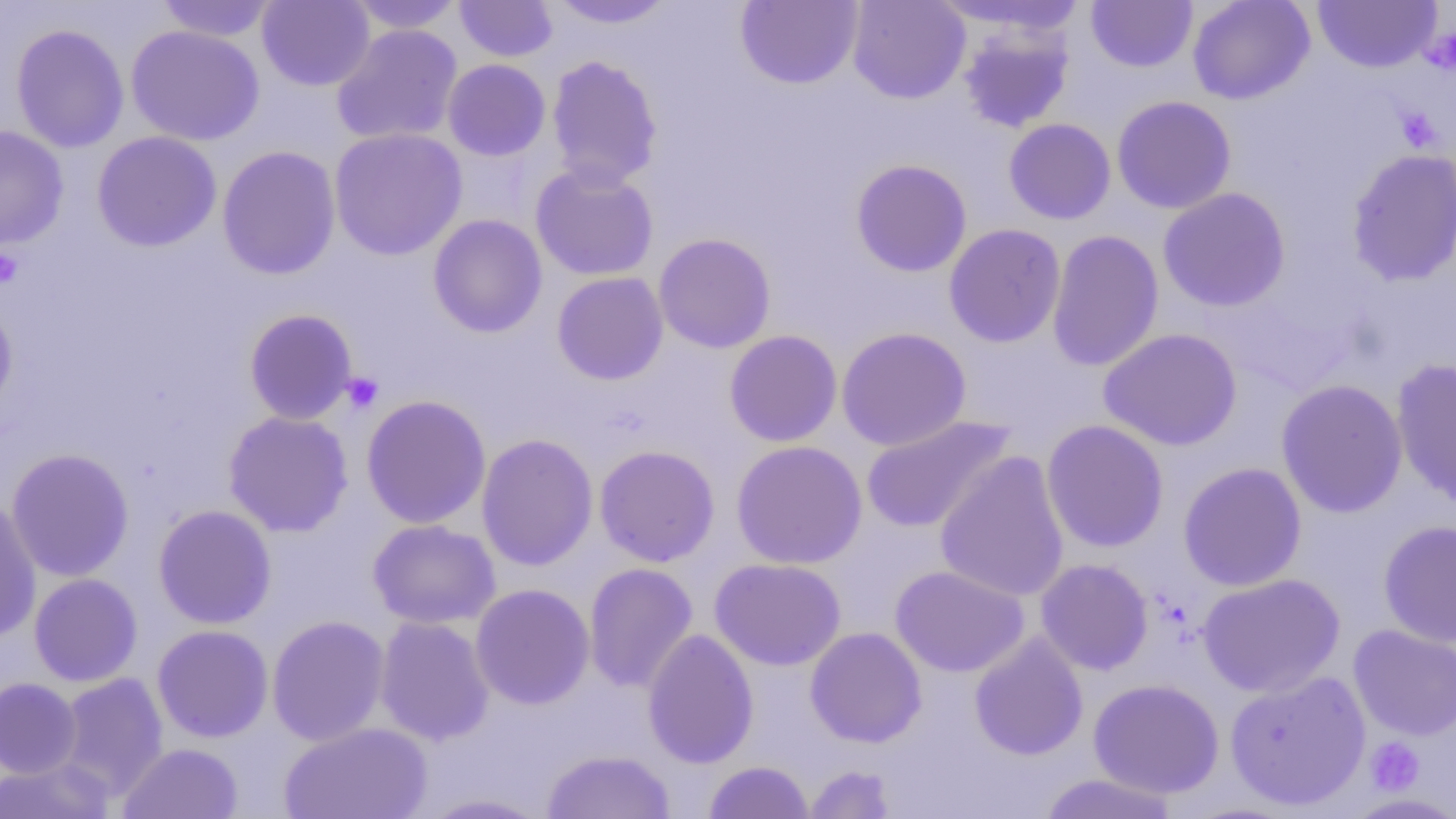

slide-level diagnosis = negative for blood parasites
platelet locations = approximate bounding boxes as (x1, y1, x2, y2) in pixels: (1422, 26, 1456, 75), (1395, 107, 1444, 152), (0, 248, 24, 289), (340, 371, 383, 414), (1365, 737, 1425, 795)
image size = 1456×819 pixels
preparation = thin blood film
uninfected red blood cell locations = approximate bounding boxes as (x1, y1, x2, y2) in pixels: (155, 0, 279, 42), (257, 0, 375, 91), (345, 0, 466, 33), (455, 0, 558, 62), (735, 0, 863, 89), (847, 0, 970, 104), (931, 0, 1093, 37), (1187, 0, 1315, 105), (1312, 0, 1442, 72), (548, 1, 677, 29), (1086, 1, 1197, 72), (11, 23, 129, 153), (957, 23, 1075, 133), (331, 24, 463, 146), (126, 25, 265, 146), (546, 55, 663, 190), (442, 59, 551, 161), (1111, 95, 1236, 214), (1003, 118, 1116, 224), (0, 125, 69, 250), (329, 128, 467, 261), (92, 131, 222, 252), (217, 145, 341, 280), (1345, 148, 1456, 286), (850, 158, 972, 277), (530, 163, 659, 281), (1158, 187, 1291, 312), (428, 214, 547, 338), (943, 223, 1066, 347), (1046, 229, 1164, 372), (653, 232, 776, 353), (552, 272, 669, 385), (0, 299, 18, 417), (244, 309, 358, 425), (836, 327, 971, 451), (1098, 328, 1242, 451), (724, 330, 842, 447), (1390, 357, 1456, 511), (1276, 379, 1408, 518), (361, 394, 492, 529), (223, 410, 354, 537), (860, 415, 1016, 534), (1041, 419, 1169, 553), (476, 433, 598, 571), (731, 440, 867, 569), (594, 444, 720, 567), (6, 448, 135, 582), (934, 450, 1070, 602), (1178, 462, 1307, 591), (0, 497, 42, 642), (153, 505, 277, 629), (368, 519, 501, 629), (1378, 520, 1456, 648), (709, 558, 846, 671), (1035, 558, 1154, 675), (583, 562, 698, 694), (891, 565, 1029, 677), (29, 573, 143, 687), (1196, 573, 1345, 698), (470, 583, 595, 710), (266, 615, 391, 746), (375, 615, 495, 746), (152, 624, 274, 742), (1348, 625, 1456, 741), (805, 626, 927, 747), (642, 628, 759, 769), (969, 633, 1088, 761), (1224, 670, 1371, 811), (57, 672, 169, 798), (0, 677, 82, 779), (1088, 678, 1224, 798), (279, 722, 434, 819), (118, 742, 244, 818), (541, 749, 676, 818), (0, 758, 116, 818), (703, 760, 814, 818), (803, 764, 897, 818), (1037, 772, 1181, 818), (419, 792, 553, 818)
modality = light microscopy
field of view = single
magnification = 1000x